Report the malaria status of this cell.
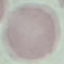

Uninfected.

Photographed with a smartphone camera at the microscope eyepiece. Giemsa stain. Cell patch, automatically extracted from a larger field of view and resized to 64 × 64 pixels. Thin blood smear.